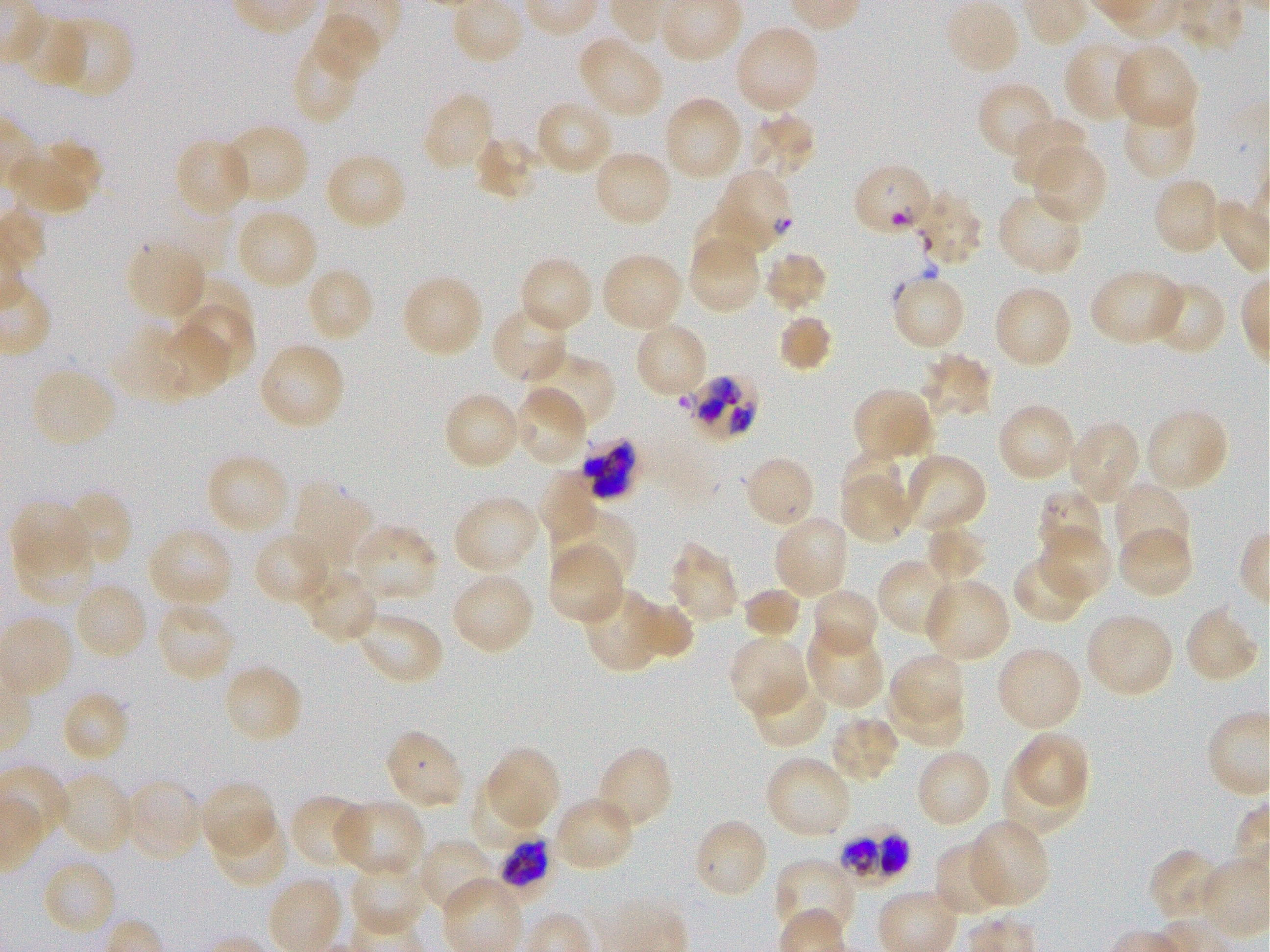 Approximate bounding boxes as (x1, y1, x2, y2) in pixels. Not every red blood cell is marked. A life-cycle stage — or a range of stages, where the recorded stages span more than one — follows each staged infected red blood cell. Locations of uninfected red blood cells: (949, 1, 1020, 71), (312, 15, 383, 83), (13, 16, 88, 91), (53, 16, 134, 99), (738, 31, 818, 111), (576, 35, 664, 119), (291, 40, 363, 124), (1064, 41, 1146, 125), (1114, 43, 1199, 130), (977, 80, 1057, 160), (662, 95, 744, 182), (423, 97, 494, 168), (1122, 98, 1198, 180), (538, 103, 610, 171), (746, 114, 818, 181), (1010, 117, 1090, 190), (221, 123, 310, 204), (472, 135, 540, 202), (8, 139, 102, 214), (177, 139, 252, 218), (1031, 143, 1107, 226), (592, 150, 673, 228), (324, 151, 408, 231), (1156, 179, 1217, 252), (999, 195, 1085, 276), (691, 207, 758, 277), (234, 209, 319, 291), (687, 236, 761, 315), (126, 239, 206, 319), (762, 250, 829, 314), (600, 252, 684, 333), (518, 256, 595, 335), (304, 266, 376, 344), (1089, 268, 1185, 347), (401, 274, 484, 358), (893, 277, 965, 347), (173, 278, 253, 340), (1154, 284, 1225, 355), (992, 285, 1074, 369), (181, 306, 254, 379), (494, 308, 564, 383), (776, 313, 835, 374), (634, 321, 709, 400), (160, 325, 232, 396), (110, 330, 194, 403), (257, 341, 345, 430), (521, 351, 616, 428), (921, 352, 995, 421), (29, 367, 118, 450), (513, 387, 586, 464), (850, 387, 933, 463), (446, 395, 517, 467), (996, 403, 1076, 483), (1144, 408, 1230, 492), (1067, 419, 1142, 505), (841, 450, 904, 503), (205, 453, 291, 537), (899, 455, 986, 532), (752, 460, 811, 523), (538, 471, 597, 545), (840, 475, 914, 544), (292, 480, 373, 569), (1114, 483, 1191, 564), (61, 489, 133, 568), (452, 495, 541, 576), (10, 501, 89, 577), (552, 507, 638, 587), (773, 514, 851, 600), (351, 523, 440, 604), (923, 523, 987, 583), (147, 526, 234, 609), (1117, 527, 1194, 600), (1040, 528, 1111, 600), (251, 532, 332, 604), (15, 535, 96, 607), (669, 543, 741, 625), (547, 545, 625, 625), (1011, 555, 1091, 625), (878, 557, 959, 639), (300, 568, 381, 643), (449, 571, 536, 656), (923, 578, 1011, 662), (79, 586, 147, 657), (582, 586, 668, 673), (741, 586, 803, 641), (813, 590, 879, 658), (629, 595, 694, 659), (1186, 599, 1259, 680), (155, 602, 236, 682), (355, 611, 444, 687), (1084, 612, 1174, 698), (805, 624, 883, 709), (729, 635, 809, 716), (995, 646, 1083, 732), (890, 653, 965, 725), (222, 664, 305, 746), (751, 674, 830, 750), (889, 683, 964, 746), (65, 693, 129, 760), (827, 714, 901, 785), (383, 728, 465, 812), (1018, 731, 1088, 807), (1001, 744, 1081, 837), (485, 745, 561, 830), (594, 745, 674, 833), (914, 747, 993, 830), (764, 755, 851, 840), (56, 771, 136, 856), (123, 779, 203, 861), (198, 780, 277, 857), (469, 782, 544, 857), (289, 793, 369, 870), (552, 795, 636, 874), (333, 799, 425, 879), (211, 813, 289, 889), (692, 817, 769, 901), (965, 820, 1051, 908), (415, 838, 498, 916), (934, 841, 1011, 917), (1146, 848, 1223, 923), (350, 857, 428, 937), (40, 858, 119, 938), (773, 858, 858, 941). Locations of red blood cells of indeterminate infection status: (855, 167, 929, 236), (915, 190, 982, 265), (579, 438, 641, 502). Locations of infected red blood cells: (715, 169, 794, 254); (679, 374, 759, 442); (1041, 490, 1101, 556); (840, 823, 910, 889); (498, 831, 553, 905) trophozoite. 100x oil-immersion objective, numerical aperture 1.25. Thin blood film. Single field of view. Image is 1270×952 pixels. Giemsa stain. Donor blood group O+. P. falciparum strain 3D7 maintained in static in-vitro culture.